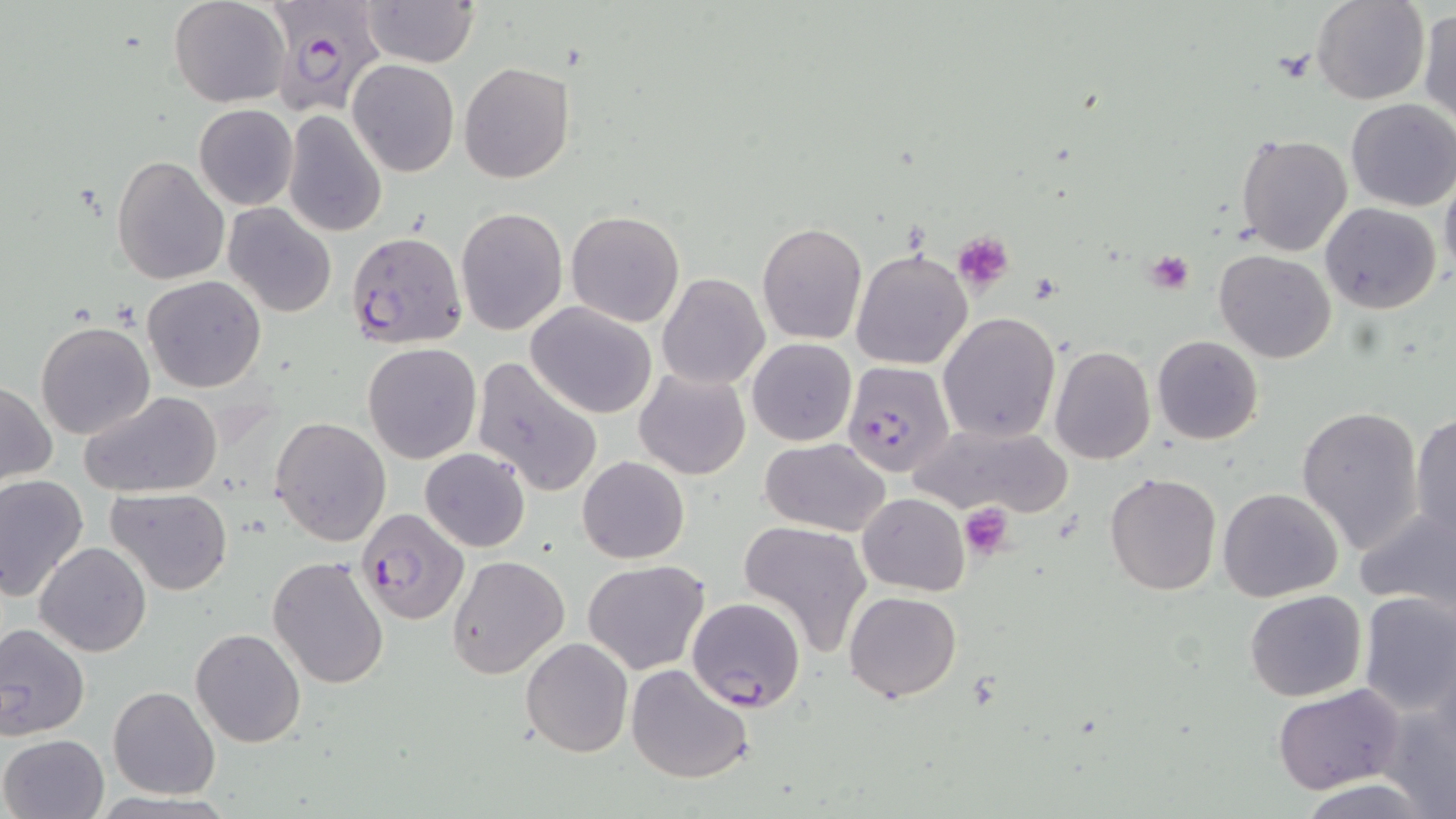

slide_level_diagnosis: Plasmodium falciparum
modality: light microscopy
field_of_view: one of a larger specimen
uninfected_red_blood_cell_locations: 'approximate bounding boxes as named x1/y1/x2/y2 corners in pixels: (x1=169, y1=0, x2=290, y2=107), (x1=361, y1=0, x2=480, y2=67), (x1=1310, y1=1, x2=1430, y2=105), (x1=1417, y1=6, x2=1455, y2=125), (x1=349, y1=60, x2=459, y2=177), (x1=458, y1=62, x2=575, y2=184), (x1=1344, y1=99, x2=1456, y2=211), (x1=193, y1=104, x2=298, y2=210), (x1=283, y1=111, x2=386, y2=237), (x1=1236, y1=134, x2=1352, y2=255), (x1=112, y1=156, x2=229, y2=284), (x1=1440, y1=167, x2=1456, y2=282), (x1=1321, y1=202, x2=1440, y2=313), (x1=225, y1=203, x2=337, y2=318), (x1=457, y1=206, x2=569, y2=336), (x1=566, y1=211, x2=686, y2=328), (x1=756, y1=222, x2=867, y2=345), (x1=850, y1=246, x2=973, y2=371), (x1=1214, y1=249, x2=1337, y2=363), (x1=657, y1=273, x2=769, y2=389), (x1=142, y1=275, x2=267, y2=393), (x1=525, y1=302, x2=658, y2=420), (x1=939, y1=312, x2=1060, y2=442), (x1=36, y1=319, x2=156, y2=440), (x1=1152, y1=334, x2=1263, y2=445), (x1=747, y1=338, x2=856, y2=446), (x1=363, y1=343, x2=482, y2=465), (x1=1049, y1=345, x2=1156, y2=465), (x1=471, y1=355, x2=603, y2=499), (x1=634, y1=368, x2=751, y2=481), (x1=1, y1=379, x2=56, y2=487), (x1=79, y1=391, x2=224, y2=499), (x1=1295, y1=406, x2=1425, y2=553), (x1=1409, y1=411, x2=1456, y2=540), (x1=269, y1=417, x2=392, y2=546), (x1=910, y1=420, x2=1072, y2=520), (x1=759, y1=437, x2=890, y2=537), (x1=421, y1=447, x2=531, y2=552), (x1=577, y1=456, x2=689, y2=564), (x1=1103, y1=471, x2=1221, y2=595), (x1=1, y1=476, x2=90, y2=603), (x1=107, y1=486, x2=232, y2=595), (x1=1218, y1=487, x2=1343, y2=601), (x1=858, y1=493, x2=969, y2=595), (x1=1354, y1=502, x2=1456, y2=611), (x1=738, y1=520, x2=873, y2=658), (x1=34, y1=542, x2=153, y2=658), (x1=267, y1=554, x2=393, y2=690), (x1=447, y1=554, x2=570, y2=680), (x1=583, y1=559, x2=710, y2=675), (x1=1244, y1=589, x2=1367, y2=702), (x1=845, y1=590, x2=962, y2=701), (x1=1357, y1=590, x2=1456, y2=716), (x1=687, y1=597, x2=805, y2=713), (x1=0, y1=620, x2=91, y2=738), (x1=190, y1=628, x2=307, y2=748), (x1=521, y1=637, x2=633, y2=757), (x1=625, y1=663, x2=757, y2=785), (x1=1272, y1=684, x2=1405, y2=793), (x1=107, y1=685, x2=222, y2=799), (x1=1376, y1=694, x2=1456, y2=818), (x1=1, y1=733, x2=108, y2=819)'
magnification: 1000x
stain: May-Grünwald-Giemsa
preparation: thin blood smear
image_size: 1456×819 pixels
platelet_locations: 'approximate bounding boxes as named x1/y1/x2/y2 corners in pixels: (x1=951, y1=230, x2=1016, y2=291), (x1=1146, y1=252, x2=1195, y2=295), (x1=959, y1=503, x2=1018, y2=558)'
plasmodium_falciparum_infected_red_blood_cell_locations: 'approximate bounding boxes as named x1/y1/x2/y2 corners in pixels: (x1=266, y1=2, x2=388, y2=114), (x1=346, y1=230, x2=468, y2=351), (x1=842, y1=361, x2=955, y2=476), (x1=355, y1=506, x2=469, y2=625)'